Look for parasitized red blood cells.
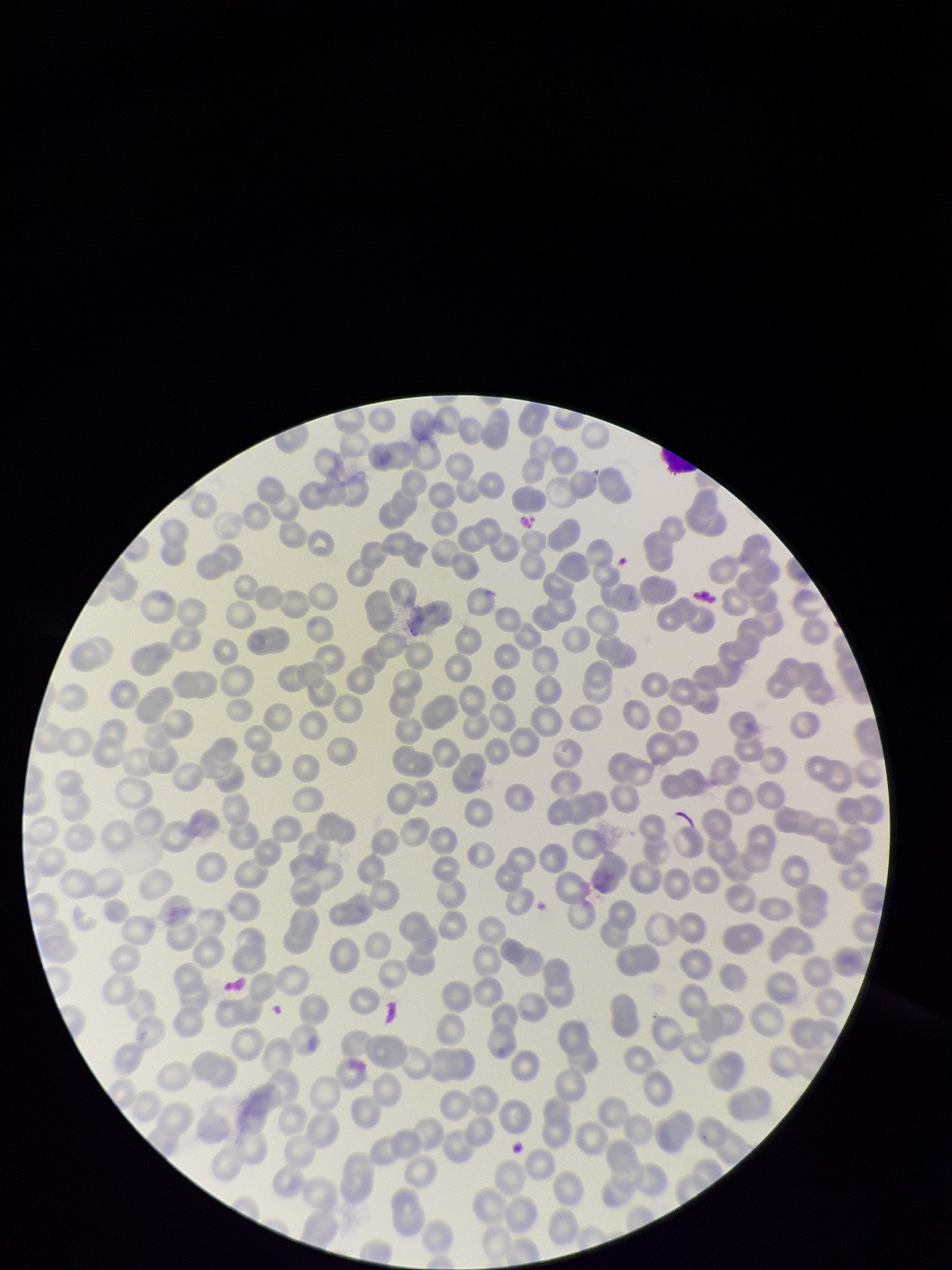

None detected.

Single field of view. Photographed through the microscope eyepiece with a smartphone camera. Preparation: thin blood smear. Parasitized red blood cell count: 0. Red blood cell count: 262. Patient malaria status: negative. Giemsa stain. Image is 952×1270 pixels.